State the preparation type.
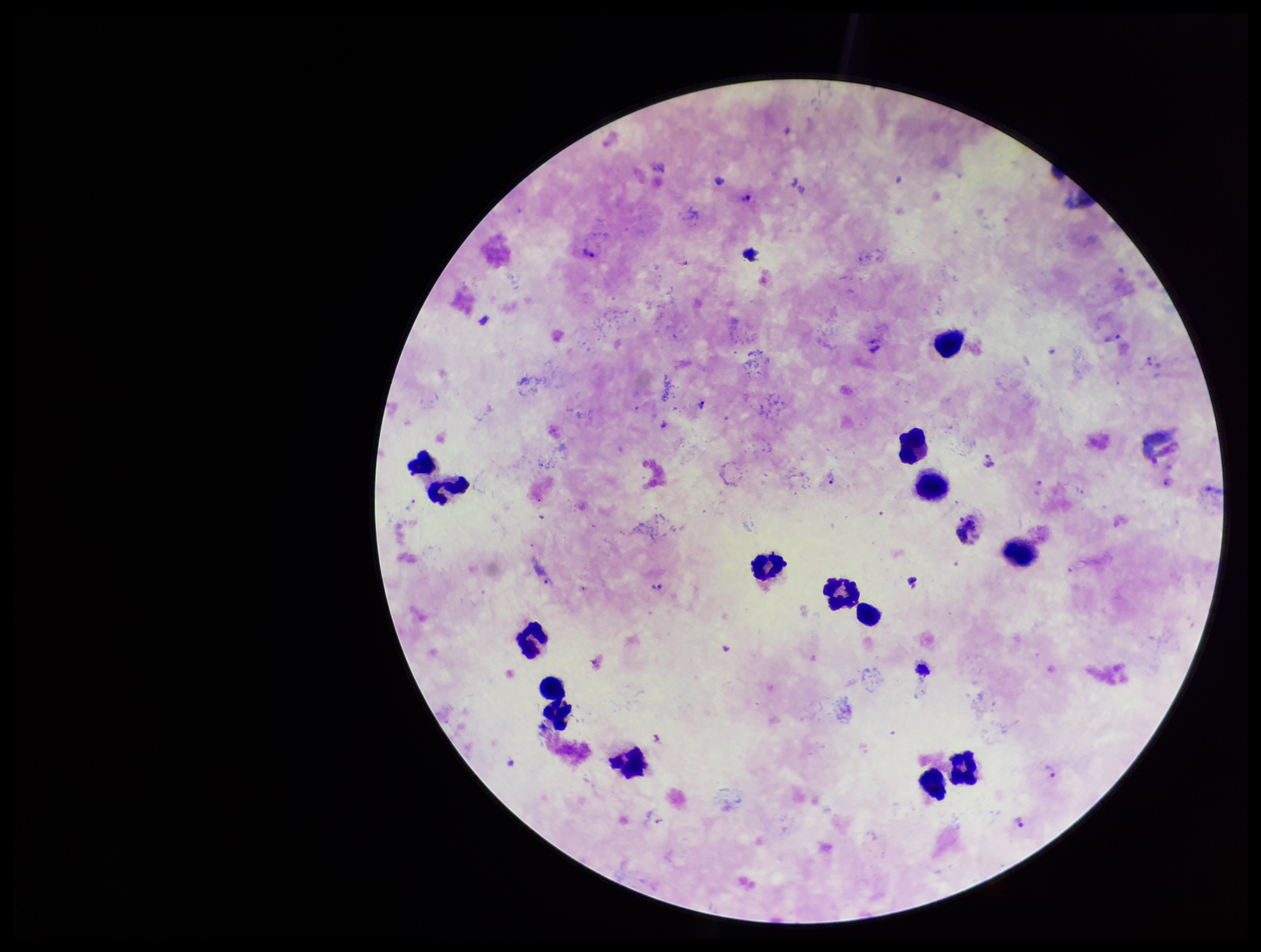
It is a thick blood smear.

Summary:
  - Capture: smartphone photograph through the microscope eyepiece
  - Leukocyte count: 14
  - Image size: 1261×952 pixels
  - Species reported for this patient: Plasmodium vivax
  - Stain: Giemsa
  - Parasite count: 10
  - Field of view: one from this slide
  - Plasmodium parasites: identified
  - Patient malaria status: positive